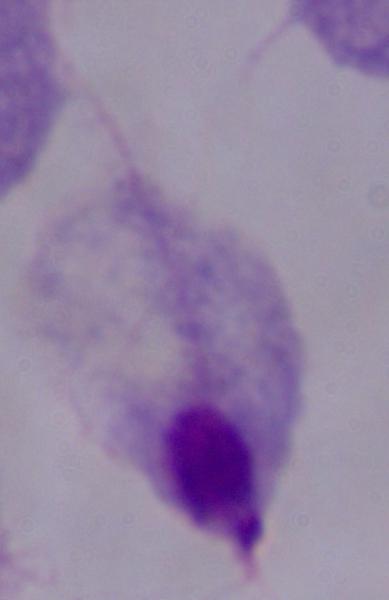
Summary:
  - Identification: trichomonad
  - Magnification: 1000x
  - Modality: photomicrograph